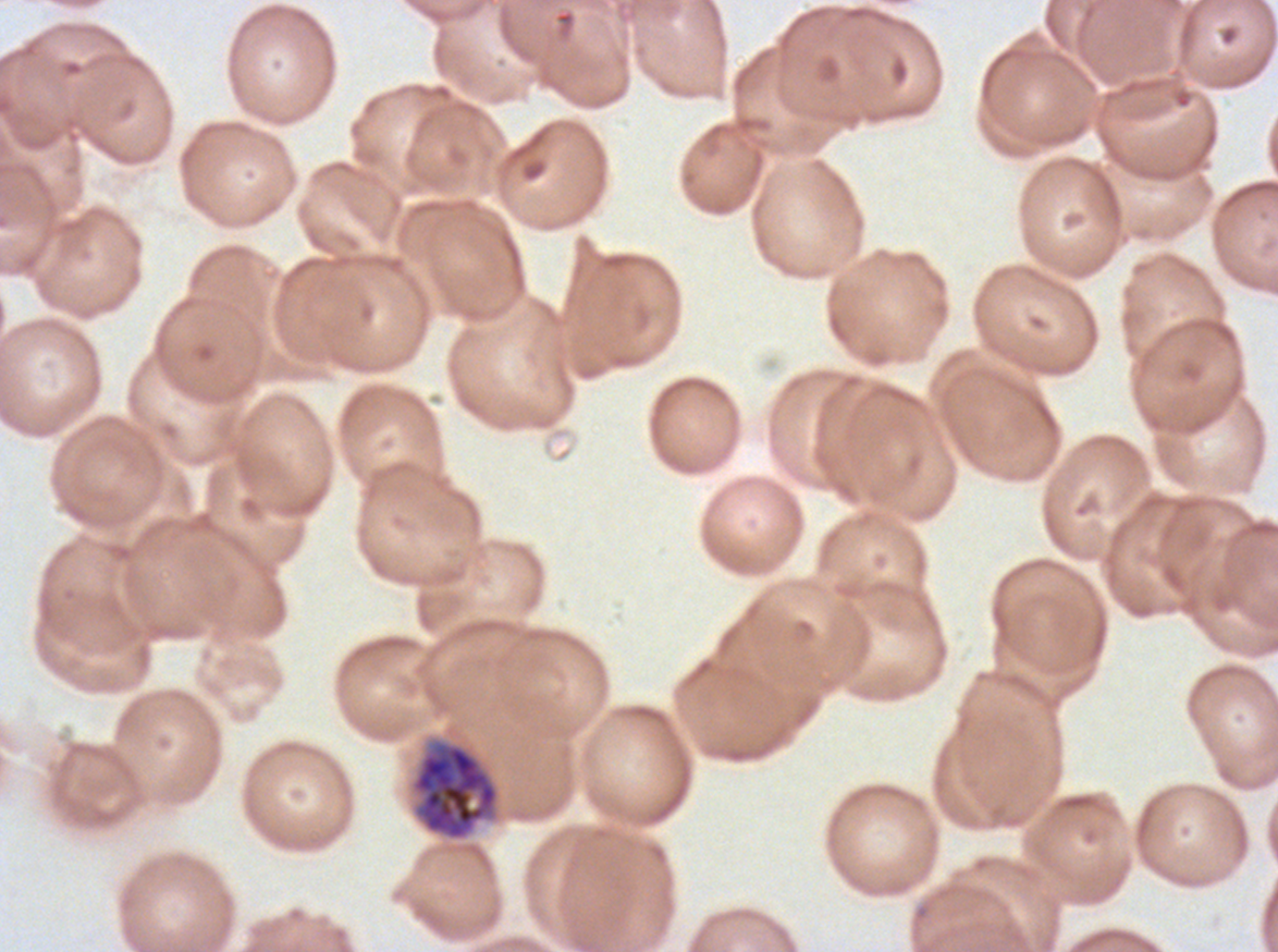
notation = approximate bounding boxes as (x1, y1, x2, y2) in pixels
late schizont locations = (409, 735, 501, 842)
image size = 1278×952 pixels
preparation = thin blood smear
field of view = sub-image separated from a larger composite
stain = Giemsa
specimen = Plasmodium falciparum cultured ex vivo for 24 to 48 hours, from a patient in The Gambia